Locate the cells, classifying each as a parasitized RBC, an uninfected RBC, or a WBC.
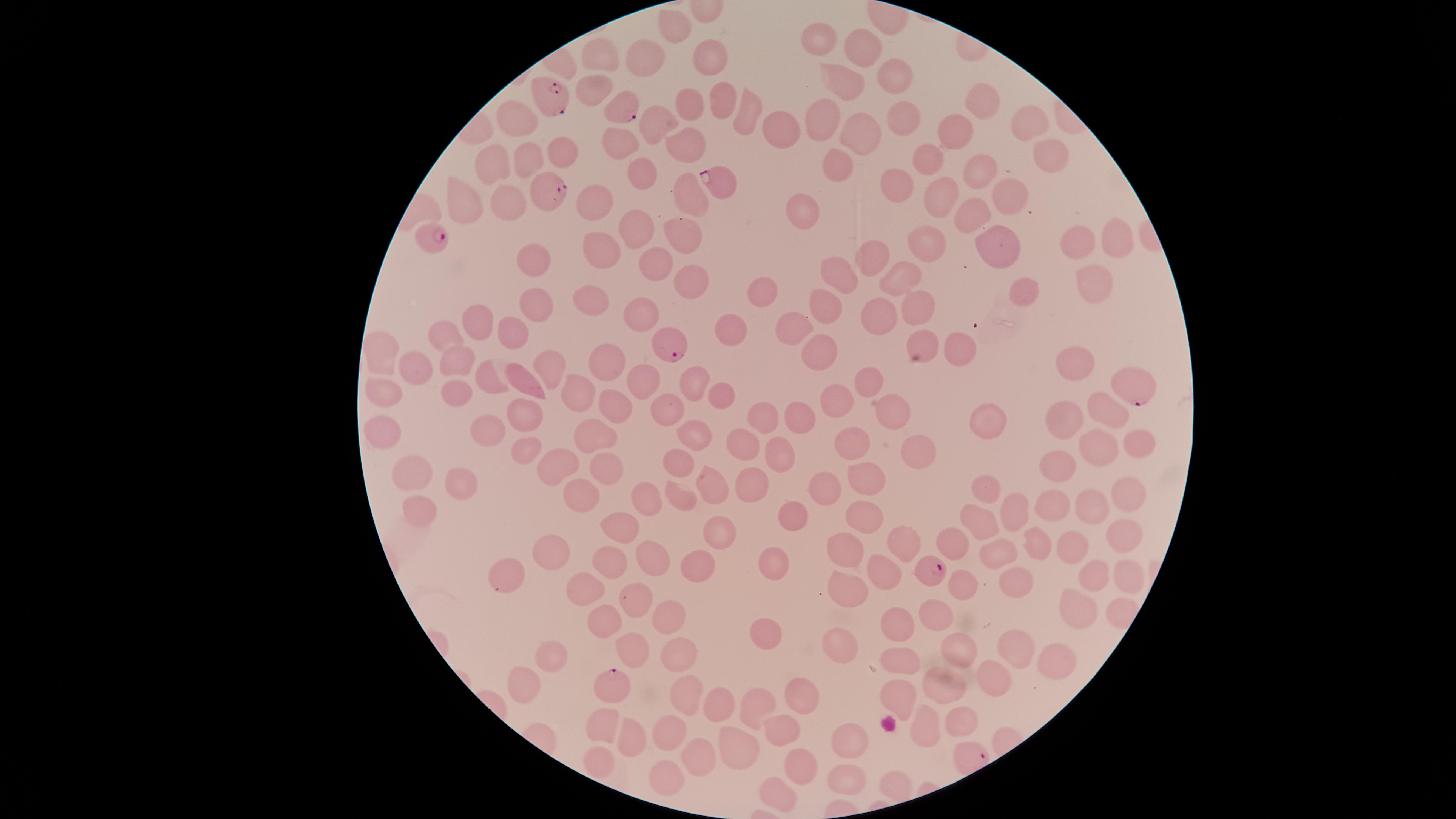
Approximate marker points as (x, y) in pixels.
Parasitized RBCs: (554, 99), (620, 111), (719, 178), (546, 187), (431, 236), (667, 343), (1137, 384), (930, 569), (614, 685).
Uninfected RBCs: (670, 23), (819, 38), (863, 47), (604, 55), (652, 55), (709, 61), (892, 72), (846, 83), (603, 86), (722, 103), (691, 107), (981, 107), (750, 112), (821, 114), (901, 118), (518, 121), (658, 122), (1030, 125), (781, 128), (860, 132), (961, 133), (616, 141), (688, 143), (1040, 147), (558, 150), (527, 158), (929, 162), (838, 164), (495, 167), (646, 171), (974, 171), (895, 180), (1006, 188), (691, 190), (473, 197), (943, 197), (510, 207), (596, 208), (801, 213), (973, 216), (638, 229), (684, 236), (1118, 237), (931, 239), (1080, 241), (994, 242), (603, 252), (870, 262), (534, 265), (653, 266), (904, 276), (838, 278), (690, 280), (1093, 284), (753, 290), (1027, 290), (590, 302), (824, 302), (536, 307), (919, 309), (646, 315), (874, 324), (474, 325), (509, 328), (793, 329), (733, 332), (446, 338), (924, 339), (953, 350), (818, 352), (382, 357), (1068, 357), (455, 362), (550, 366), (611, 371), (410, 375), (695, 381), (528, 382), (494, 384), (866, 387), (459, 388), (646, 388), (386, 393), (579, 395), (718, 399), (832, 399), (613, 404), (1111, 407), (670, 409), (894, 410), (521, 415), (1064, 418), (761, 420), (800, 422), (987, 422), (385, 429), (491, 432), (595, 432), (695, 433), (1139, 441), (1102, 444), (745, 445), (855, 447), (915, 450), (521, 453), (777, 453), (1064, 459), (679, 460), (608, 468), (563, 470), (411, 472), (866, 479), (827, 482), (458, 484), (713, 485), (994, 486), (748, 488), (1121, 494), (581, 496), (680, 499), (646, 502), (1056, 504), (1091, 505), (1021, 509), (860, 513), (421, 514), (978, 517), (793, 520), (620, 528), (896, 529), (717, 530), (954, 536), (1121, 539), (1038, 542), (551, 547), (1073, 548), (851, 549), (997, 555), (658, 558), (692, 559), (608, 560), (777, 565), (883, 571), (1096, 573), (507, 575), (1017, 579), (1132, 582), (846, 584), (583, 585), (961, 587), (636, 595), (1080, 601), (671, 611), (895, 611), (602, 617), (936, 617), (765, 634), (1018, 645), (631, 647), (959, 648), (676, 650), (556, 652), (843, 652), (1047, 657), (904, 663), (999, 677), (522, 680), (944, 684), (686, 686), (807, 694), (898, 698), (722, 702), (747, 711), (954, 714), (605, 724), (917, 726), (780, 731), (670, 732), (636, 738), (847, 738), (734, 746), (699, 754), (599, 760), (791, 772), (668, 776), (841, 778), (896, 789), (779, 799).
No WBCs identified.

Species: Plasmodium falciparum. The visible region is circular. Giemsa stain. Smartphone photograph through the microscope eyepiece. One field of view of the specimen. Thin smear of blood. Image is 1456×819 pixels.